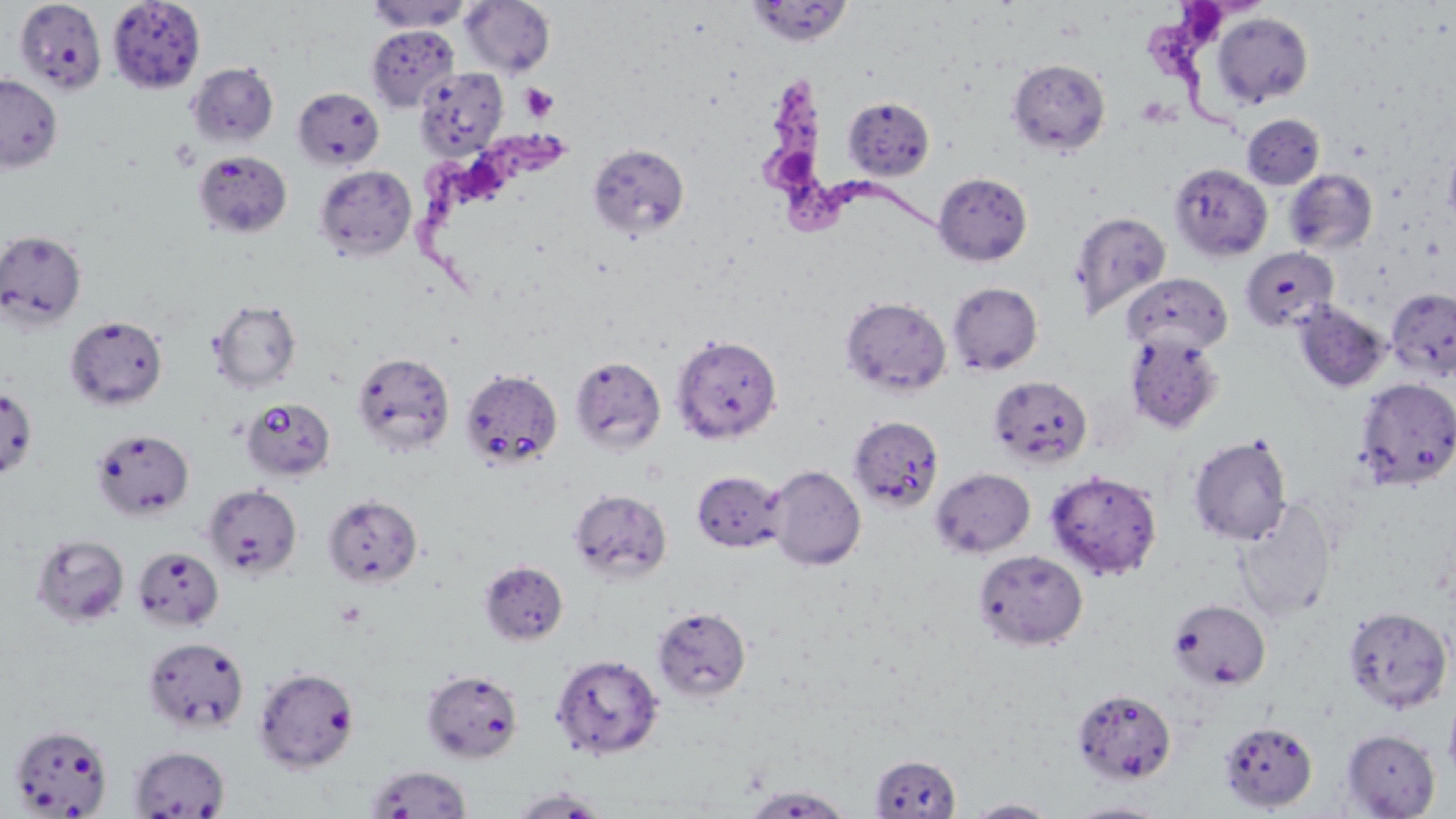
slide_level_diagnosis: Trypanosoma brucei
image_size: 1456×819 pixels
field_of_view: single
preparation: thin blood smear
stain: May-Grünwald-Giemsa
platelet_locations: 'approximate bounding boxes as [x1, y1, x2, y2] in pixels: [520, 82, 559, 123]'
modality: optical microscopy
uninfected_red_blood_cell_locations: 'approximate bounding boxes as [x1, y1, x2, y2] in pixels: [13, 0, 107, 94], [367, 0, 472, 32], [460, 0, 556, 77], [746, 0, 853, 46], [107, 1, 205, 95], [1212, 13, 1313, 108], [366, 25, 459, 112], [1007, 58, 1111, 155], [187, 62, 279, 148], [414, 67, 509, 159], [0, 73, 63, 173], [293, 87, 384, 170], [843, 97, 935, 180], [1242, 114, 1325, 189], [1443, 140, 1456, 234], [588, 143, 690, 240], [193, 150, 292, 239], [1169, 163, 1273, 262], [314, 165, 417, 262], [1284, 169, 1378, 255], [934, 172, 1032, 265], [1070, 210, 1170, 320], [0, 230, 87, 330], [1240, 247, 1339, 333], [1122, 273, 1232, 356], [948, 281, 1043, 375], [1385, 288, 1456, 381], [840, 296, 951, 397], [209, 299, 302, 393], [1293, 301, 1390, 394], [65, 315, 168, 410], [1124, 332, 1226, 434], [671, 333, 782, 444], [352, 351, 455, 457], [569, 356, 666, 453], [460, 368, 562, 469], [988, 376, 1092, 469], [1354, 378, 1456, 490], [0, 387, 38, 479], [240, 398, 336, 481], [848, 416, 943, 511], [91, 428, 195, 520], [1188, 433, 1293, 546], [768, 465, 866, 571], [931, 468, 1035, 558], [1045, 469, 1163, 580], [691, 470, 786, 553], [202, 484, 302, 579], [568, 488, 672, 584], [323, 495, 423, 588], [1234, 499, 1337, 622], [31, 533, 130, 627], [132, 546, 224, 630], [973, 549, 1088, 650], [479, 560, 568, 646], [1169, 600, 1271, 690], [1342, 605, 1453, 714], [652, 606, 751, 703], [143, 636, 250, 735], [551, 653, 664, 760], [253, 667, 359, 772], [422, 669, 523, 763], [1071, 688, 1177, 785], [1445, 690, 1456, 786], [1218, 720, 1318, 812], [9, 724, 113, 817], [1341, 729, 1441, 818], [127, 745, 231, 818], [869, 754, 961, 818], [363, 765, 473, 817], [742, 785, 854, 817], [508, 788, 610, 817], [965, 799, 1057, 817], [1064, 801, 1171, 818]'
magnification: 1000x
trypanosoma_brucei_locations: 'approximate bounding boxes as [x1, y1, x2, y2] in pixels: [1146, 0, 1260, 136], [760, 76, 940, 237], [410, 121, 571, 293]'